Assess this cell for malaria.
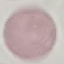

Uninfected.

Automatically extracted cell patch, resized to 64 × 64 pixels. Photographed with a smartphone camera at the microscope eyepiece. Giemsa-stained preparation. Thin blood film.